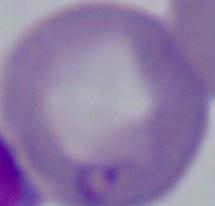

Summary:
  - Modality: micrograph
  - Identification: Babesia
  - Magnification: 1000x